Point out each Plasmodium parasite.
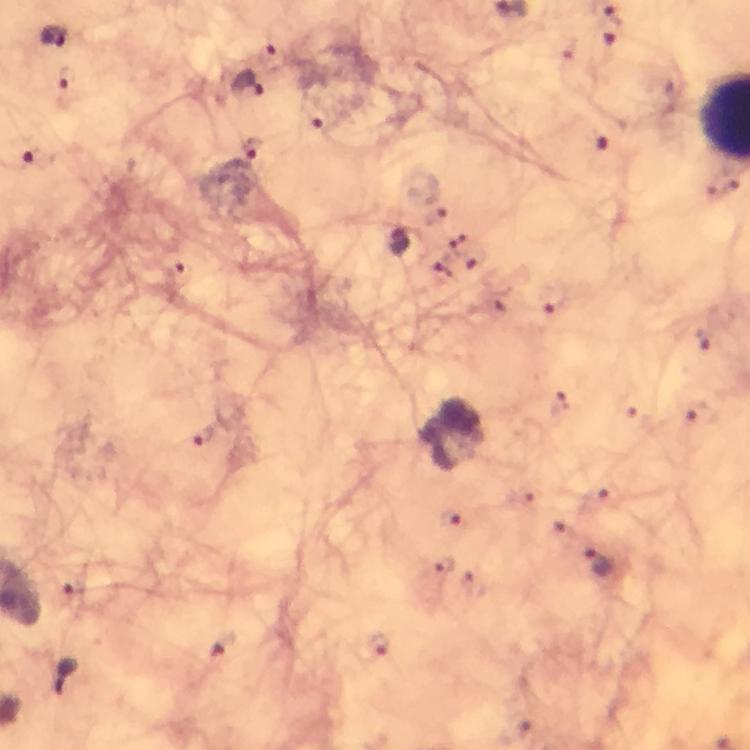
Approximate object centers, in pixels from the top-left corner.
Plasmodium parasites: (x=54, y=36), (x=609, y=40), (x=268, y=54), (x=66, y=80), (x=243, y=84), (x=316, y=117), (x=597, y=140), (x=251, y=149), (x=36, y=160), (x=723, y=185), (x=398, y=240), (x=179, y=276), (x=440, y=276), (x=553, y=306), (x=703, y=337), (x=558, y=403), (x=626, y=404), (x=693, y=411), (x=205, y=436), (x=600, y=496), (x=450, y=518), (x=597, y=564), (x=444, y=566), (x=474, y=581), (x=74, y=589), (x=221, y=644), (x=377, y=644).

cropped from = a single field of view
context = from a malaria diagnostic workup
preparation = thick blood film
immersion oil = applied
magnification = 100x
stain = Giemsa
image size = 750×750 pixels
capture = smartphone camera through the microscope